Identify the blood parasite species.
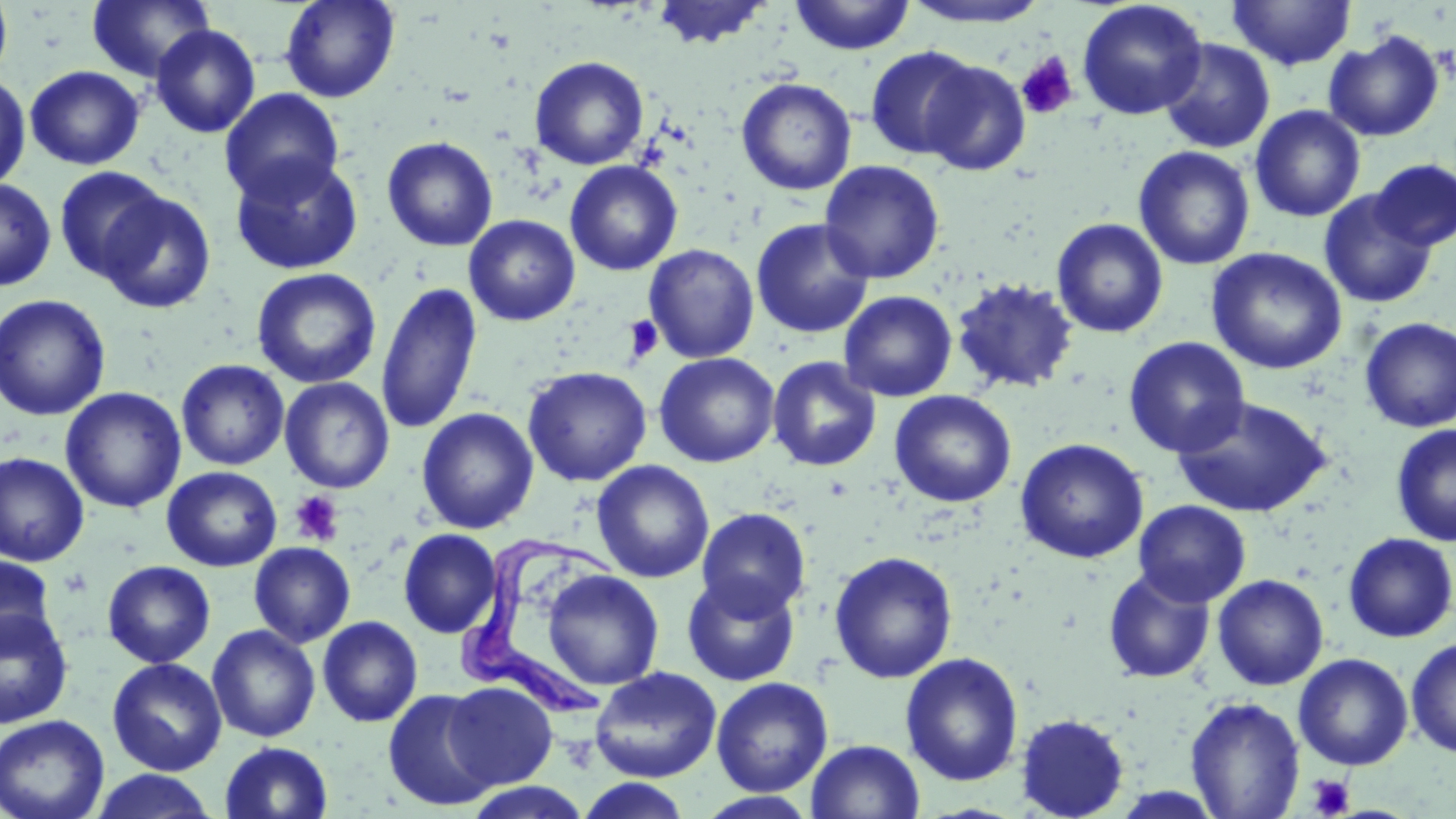
Trypanosoma brucei.

uninfected red blood cell locations = approximate bounding boxes as (x1, y1, x2, y2) in pixels: (0, 0, 13, 85), (87, 0, 215, 83), (279, 0, 400, 103), (651, 0, 772, 49), (790, 0, 915, 56), (1076, 0, 1208, 120), (1227, 0, 1356, 71), (900, 1, 1053, 28), (150, 24, 261, 138), (1323, 30, 1445, 142), (1158, 38, 1275, 154), (864, 45, 982, 160), (529, 55, 650, 170), (918, 59, 1031, 176), (25, 65, 145, 170), (0, 71, 31, 191), (735, 77, 857, 196), (219, 88, 344, 203), (1249, 104, 1366, 222), (382, 136, 498, 252), (1133, 145, 1255, 270), (230, 153, 364, 275), (1371, 158, 1456, 251), (818, 159, 945, 284), (564, 161, 683, 276), (53, 165, 170, 283), (0, 178, 57, 291), (95, 189, 216, 314), (1318, 189, 1437, 308), (464, 215, 580, 326), (1051, 217, 1169, 339), (751, 218, 874, 339), (643, 244, 760, 363), (1206, 247, 1348, 375), (251, 267, 382, 389), (951, 277, 1079, 394), (376, 281, 483, 436), (838, 290, 957, 402), (0, 294, 111, 421), (1359, 317, 1456, 432), (1122, 337, 1250, 458), (654, 352, 779, 468), (767, 356, 881, 471), (176, 359, 290, 470), (522, 366, 652, 486), (279, 377, 395, 493), (60, 386, 186, 514), (889, 390, 1017, 507), (1172, 396, 1332, 518), (417, 407, 539, 534), (1390, 424, 1456, 546), (1015, 438, 1149, 564), (0, 452, 90, 567), (591, 460, 714, 583), (162, 466, 282, 572), (1133, 500, 1251, 607), (696, 507, 811, 618), (398, 529, 502, 638), (1342, 532, 1456, 643), (249, 541, 356, 648), (828, 550, 959, 684), (0, 552, 57, 656), (102, 560, 216, 668), (1102, 568, 1216, 684), (542, 569, 664, 690), (681, 573, 801, 687), (1212, 574, 1329, 690), (0, 605, 74, 729), (317, 615, 423, 727), (207, 624, 321, 742), (1405, 636, 1456, 758), (900, 652, 1023, 787), (1293, 653, 1413, 771), (107, 657, 227, 776), (589, 666, 722, 782), (711, 677, 833, 797), (444, 681, 559, 790), (382, 689, 501, 812), (1185, 696, 1305, 818), (1015, 713, 1129, 819), (0, 715, 109, 819), (806, 739, 925, 819), (219, 741, 333, 819), (90, 769, 220, 819), (572, 777, 696, 819), (696, 791, 820, 818)
Trypanosoma brucei locations = approximate bounding boxes as (x1, y1, x2, y2) in pixels: (455, 543, 622, 723)
platelet locations = approximate bounding boxes as (x1, y1, x2, y2) in pixels: (1016, 53, 1079, 120), (623, 314, 663, 364), (290, 490, 345, 546), (1307, 774, 1354, 818)
stain = May-Grünwald-Giemsa
field of view = single
modality = optical microscopy
image size = 1456×819 pixels
preparation = thin blood film
magnification = 1000x